Identify the preparation type.
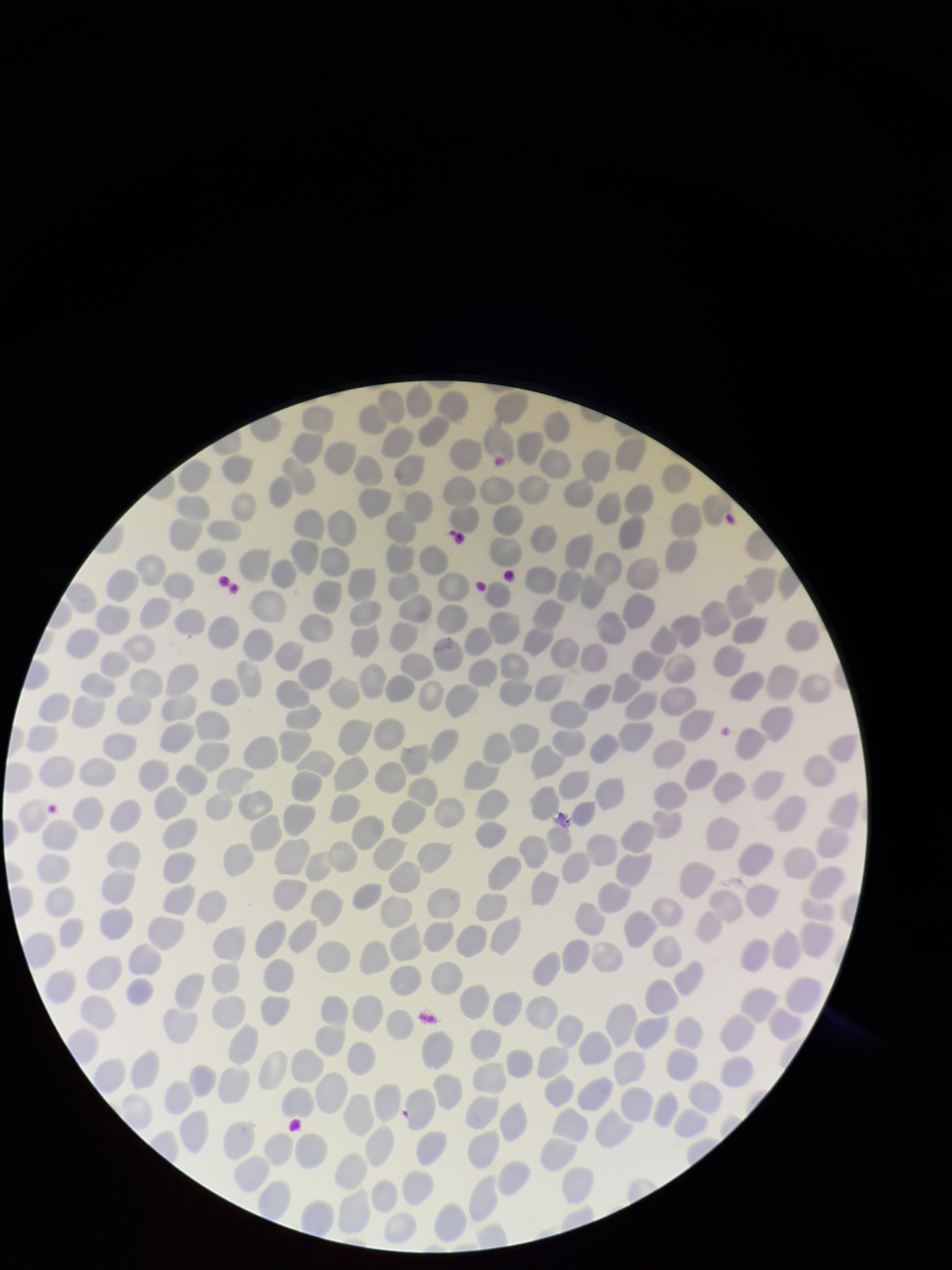
Thin.

Single field of view. Smartphone photograph taken through the eyepiece of a microscope. Patient malaria status: infected. Parasitized red blood cells: none seen. Species reported for this patient: Plasmodium falciparum. Parasitized red blood cell count: 0. Image is 952×1270 pixels. Giemsa stain. Red blood cell count: 300.